Assess the morphology of the red blood cells.
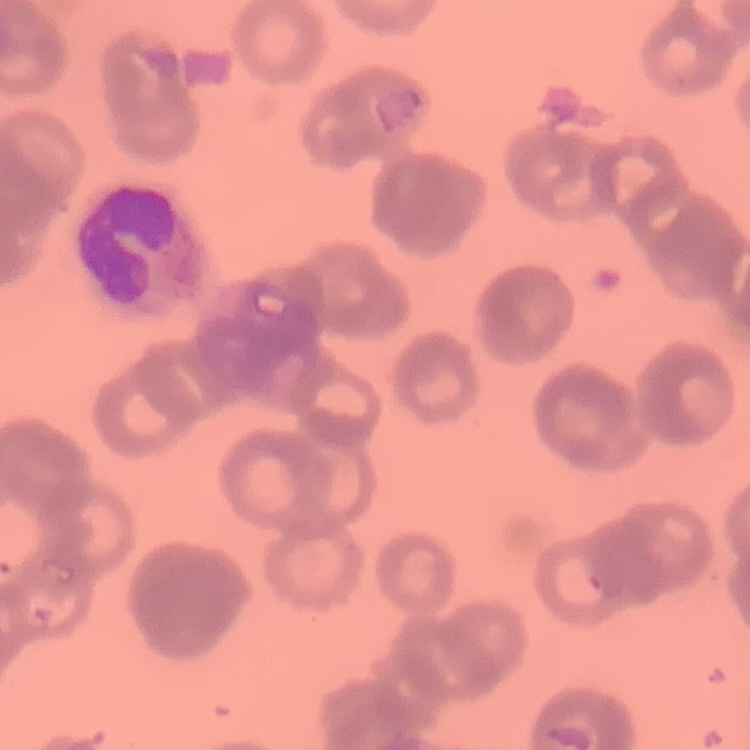
Rouleaux formation.

stain = Field's or Giemsa
image type = square crop of a larger photomicrograph
preparation = thin peripheral smear